Assess the morphology of the red blood cells.
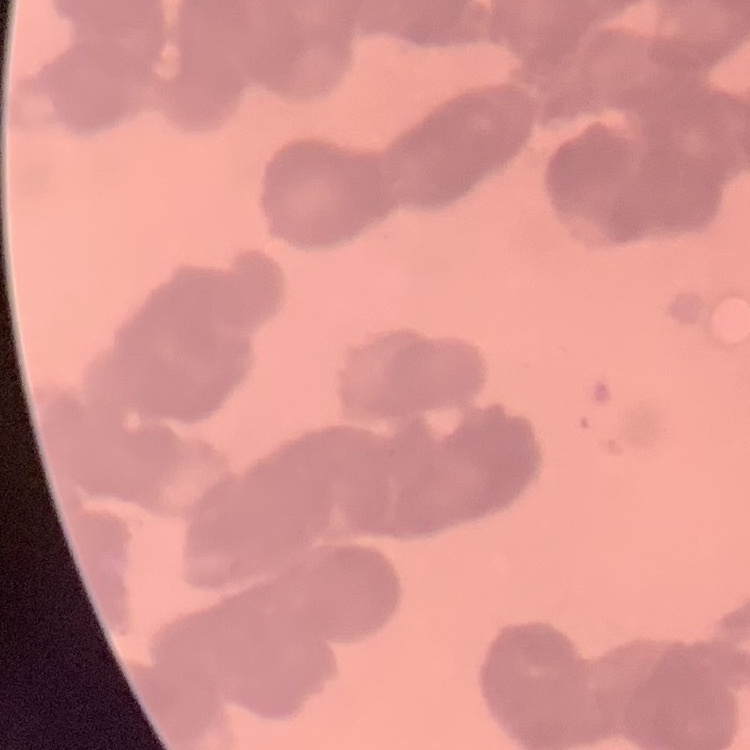
Rouleaux formation.

stain: Field's or Giemsa
image_type: one tile cut from a larger photomicrograph
preparation: thin blood film